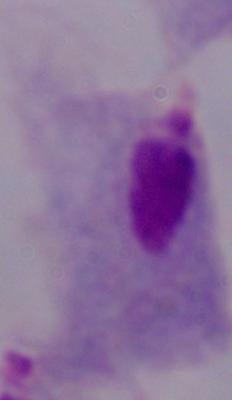
modality: photomicrograph
magnification: 1000x
identification: trichomonad